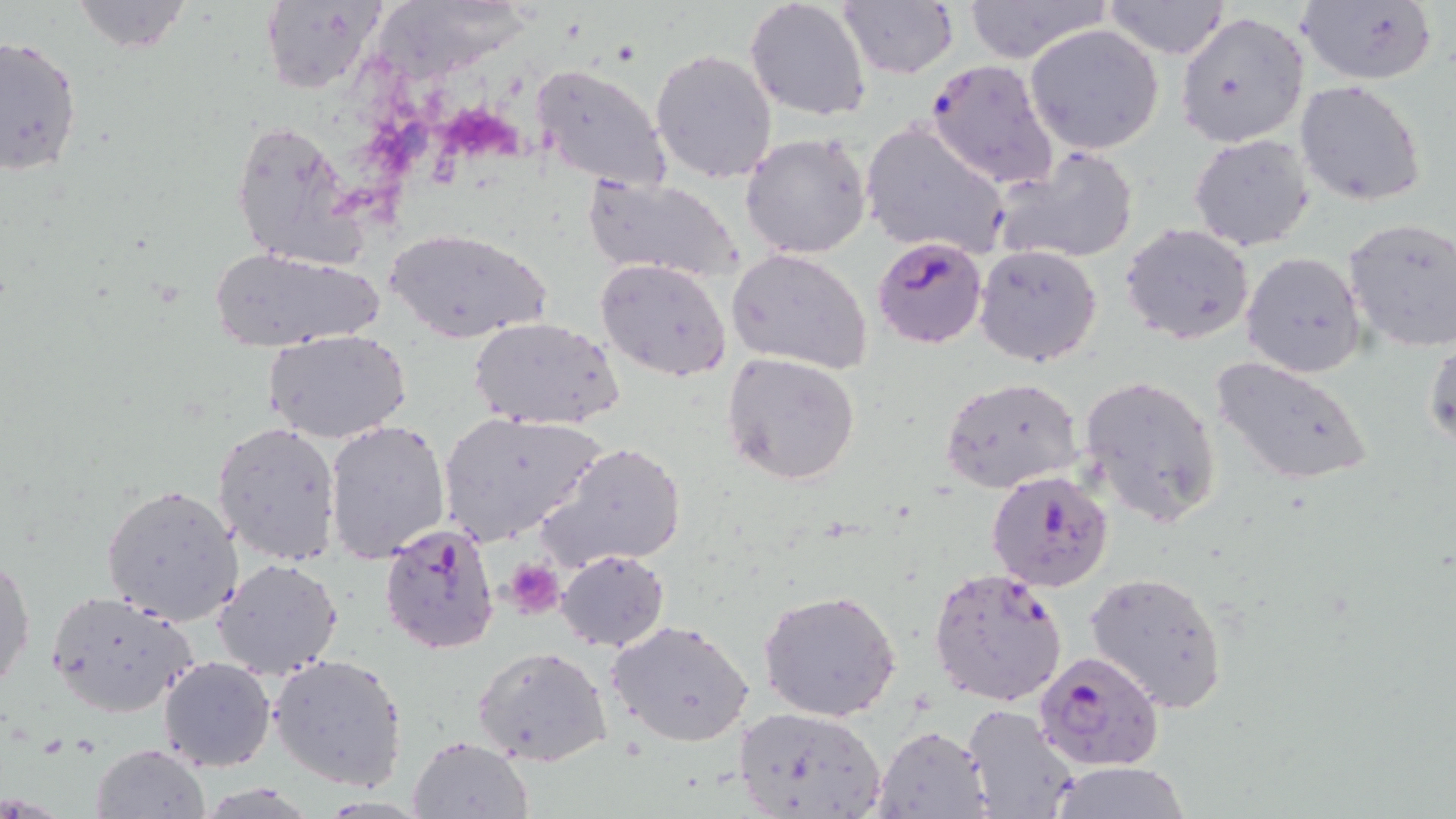

Summary:
  - Coordinate format: approximate bounding boxes as (x1,y1)-(x2,y2) corner pairs in pixels
  - Platelet locations: (505,559)-(564,619)
  - Uninfected red blood cell locations: (67,0)-(194,53), (744,0)-(872,120), (960,0)-(1111,65), (1296,0)-(1440,86), (257,1)-(383,96), (1101,1)-(1233,60), (837,2)-(959,80), (373,7)-(520,90), (1174,12)-(1310,148), (1024,24)-(1166,154), (0,32)-(83,179), (649,47)-(778,183), (530,63)-(671,192), (1294,79)-(1426,206), (230,117)-(362,271), (861,121)-(1010,260), (740,131)-(874,260), (1188,132)-(1316,251), (995,145)-(1141,264), (582,174)-(744,283), (1344,218)-(1456,354), (1121,223)-(1255,345), (386,228)-(553,344), (973,243)-(1103,368), (209,246)-(386,351), (726,247)-(875,374), (1240,251)-(1366,377), (595,259)-(732,384), (469,316)-(624,430), (263,329)-(413,443), (1424,334)-(1455,452), (722,352)-(860,485), (1210,354)-(1373,486), (1078,373)-(1222,529), (939,375)-(1083,495), (437,410)-(607,547), (211,420)-(342,566), (320,420)-(446,565), (538,441)-(687,571), (100,484)-(244,625), (555,549)-(669,651), (0,552)-(35,696), (212,557)-(343,680), (1085,569)-(1229,711), (47,589)-(198,716), (759,589)-(902,723), (608,620)-(754,748), (472,645)-(612,768), (269,654)-(407,791), (157,656)-(274,772), (733,704)-(887,819), (960,704)-(1082,819), (874,724)-(992,817), (407,734)-(533,818), (88,743)-(213,819), (1045,762)-(1194,818)
  - Plasmodium falciparum-infected red blood cell locations: (925,58)-(1058,189), (872,237)-(988,349), (984,469)-(1114,592), (376,522)-(502,655), (928,565)-(1068,707), (1030,648)-(1165,772)
  - Slide-level diagnosis: Plasmodium falciparum
  - Image size: 1456×819 pixels
  - Magnification: 1000x
  - Modality: light microscopy
  - Stain: May-Grünwald-Giemsa
  - Preparation: thin blood smear
  - Field of view: one of a larger specimen